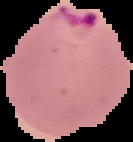

image type = cell region segmented out of the field of view; surrounding area masked to black
image size = 133×142 pixels
malaria status = parasitized
preparation = thin blood film